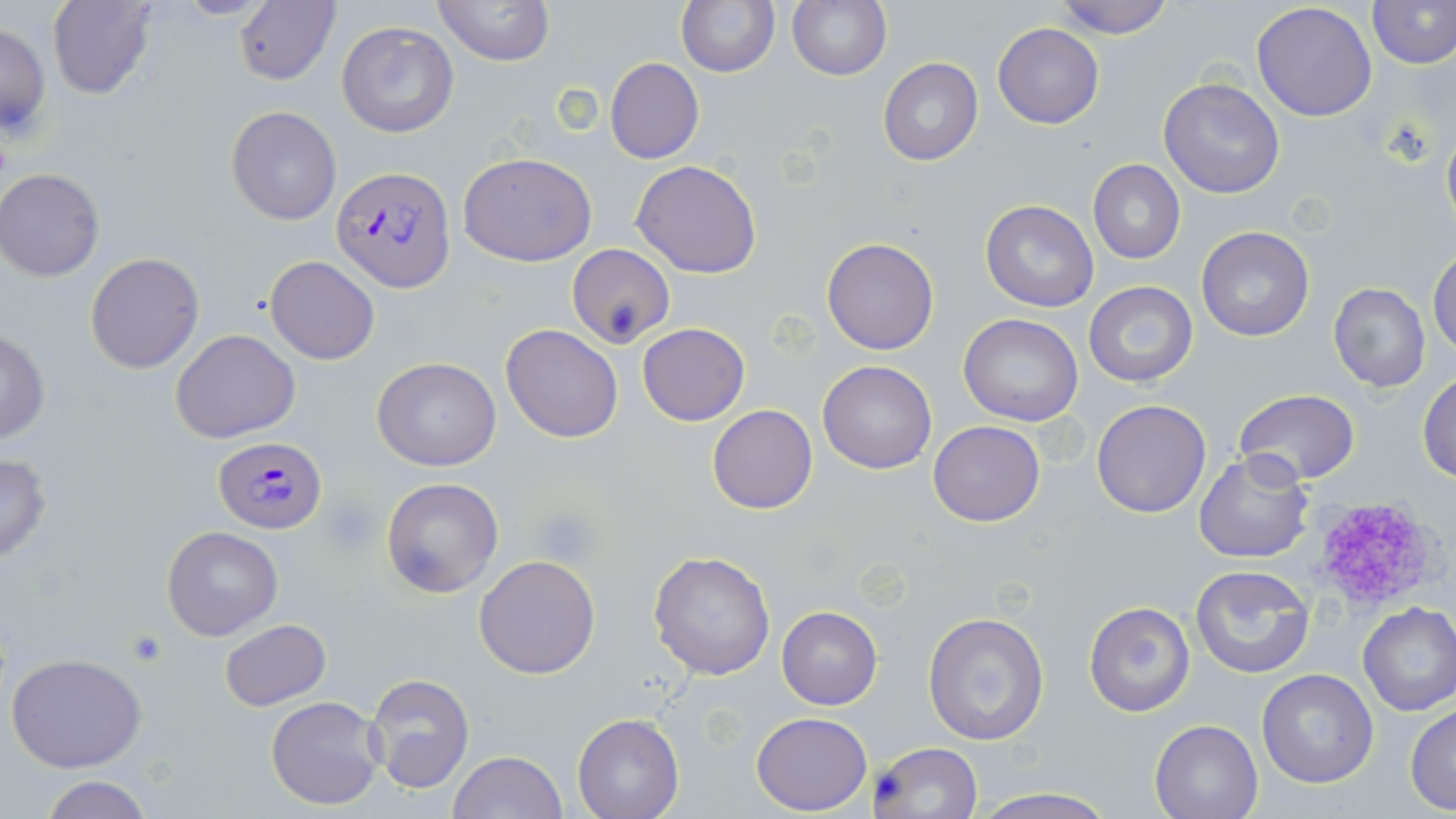
Summary:
  - Coordinate format: approximate bounding boxes as named x1/y1/x2/y2 corners in pixels
  - Plasmodium falciparum-infected red blood cell locations: (x1=332, y1=166, x2=455, y2=292), (x1=214, y1=436, x2=325, y2=532)
  - Platelet locations: (x1=1308, y1=493, x2=1442, y2=612), (x1=323, y1=497, x2=379, y2=550), (x1=533, y1=508, x2=598, y2=564), (x1=125, y1=632, x2=169, y2=666)
  - Uninfected red blood cell locations: (x1=46, y1=0, x2=156, y2=101), (x1=432, y1=0, x2=554, y2=66), (x1=676, y1=0, x2=779, y2=78), (x1=787, y1=0, x2=892, y2=81), (x1=1051, y1=0, x2=1177, y2=39), (x1=1368, y1=1, x2=1456, y2=69), (x1=234, y1=2, x2=340, y2=85), (x1=1251, y1=2, x2=1378, y2=121), (x1=0, y1=20, x2=51, y2=139), (x1=336, y1=20, x2=460, y2=139), (x1=993, y1=23, x2=1104, y2=129), (x1=877, y1=57, x2=983, y2=166), (x1=604, y1=58, x2=705, y2=164), (x1=1159, y1=77, x2=1285, y2=198), (x1=226, y1=105, x2=343, y2=226), (x1=1441, y1=112, x2=1456, y2=239), (x1=459, y1=152, x2=598, y2=267), (x1=631, y1=160, x2=763, y2=278), (x1=1088, y1=160, x2=1184, y2=264), (x1=0, y1=170, x2=104, y2=281), (x1=980, y1=200, x2=1100, y2=313), (x1=1197, y1=226, x2=1314, y2=341), (x1=822, y1=238, x2=940, y2=355), (x1=567, y1=243, x2=675, y2=349), (x1=1429, y1=246, x2=1456, y2=360), (x1=84, y1=252, x2=204, y2=374), (x1=265, y1=256, x2=380, y2=365), (x1=1083, y1=282, x2=1198, y2=386), (x1=1328, y1=283, x2=1431, y2=393), (x1=959, y1=312, x2=1083, y2=427), (x1=501, y1=323, x2=623, y2=442), (x1=638, y1=323, x2=749, y2=426), (x1=0, y1=328, x2=50, y2=446), (x1=172, y1=329, x2=299, y2=443), (x1=373, y1=356, x2=502, y2=471), (x1=817, y1=359, x2=937, y2=474), (x1=1417, y1=371, x2=1456, y2=483), (x1=1232, y1=388, x2=1360, y2=486), (x1=1091, y1=399, x2=1212, y2=519), (x1=707, y1=405, x2=817, y2=514), (x1=929, y1=421, x2=1044, y2=527), (x1=1193, y1=451, x2=1315, y2=564), (x1=0, y1=452, x2=53, y2=564), (x1=380, y1=477, x2=504, y2=598), (x1=163, y1=526, x2=282, y2=642), (x1=647, y1=548, x2=777, y2=682), (x1=474, y1=554, x2=602, y2=679), (x1=1189, y1=564, x2=1316, y2=679), (x1=1083, y1=601, x2=1195, y2=717), (x1=1357, y1=602, x2=1456, y2=716), (x1=776, y1=607, x2=884, y2=710), (x1=922, y1=609, x2=1050, y2=745), (x1=219, y1=618, x2=331, y2=710), (x1=5, y1=653, x2=149, y2=773), (x1=1256, y1=669, x2=1379, y2=789), (x1=363, y1=673, x2=475, y2=793), (x1=265, y1=695, x2=385, y2=811), (x1=1406, y1=705, x2=1456, y2=814), (x1=750, y1=711, x2=872, y2=815), (x1=573, y1=712, x2=684, y2=819), (x1=1150, y1=719, x2=1263, y2=819), (x1=870, y1=741, x2=983, y2=819), (x1=447, y1=751, x2=566, y2=819), (x1=36, y1=776, x2=158, y2=819), (x1=969, y1=785, x2=1118, y2=819)
  - Slide-level diagnosis: Plasmodium falciparum
  - Field of view: single
  - Preparation: thin blood smear
  - Modality: optical microscopy
  - Stain: May-Grünwald-Giemsa
  - Magnification: 1000x
  - Image size: 1456×819 pixels